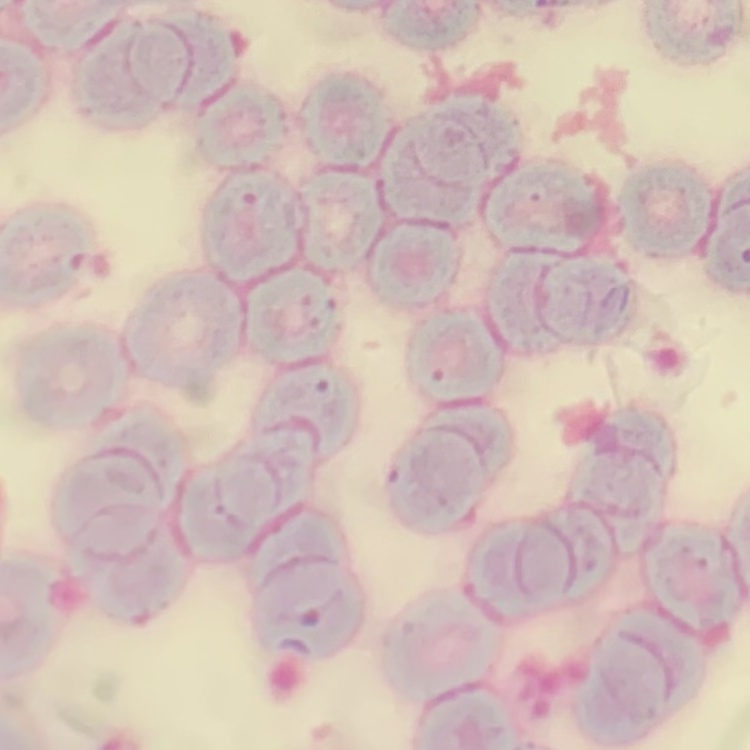

red_blood_cell_morphology: rouleaux formation
image_type: square crop of a larger photomicrograph
preparation: thin blood smear
stain: Field's or Giemsa